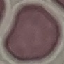

Summary:
  - Malaria status: uninfected
  - Stain: Giemsa
  - Preparation: thin blood film
  - Image type: automatically extracted cell patch, resized to 64 × 64 pixels
  - Capture: smartphone camera at the microscope eyepiece